Locate platelets.
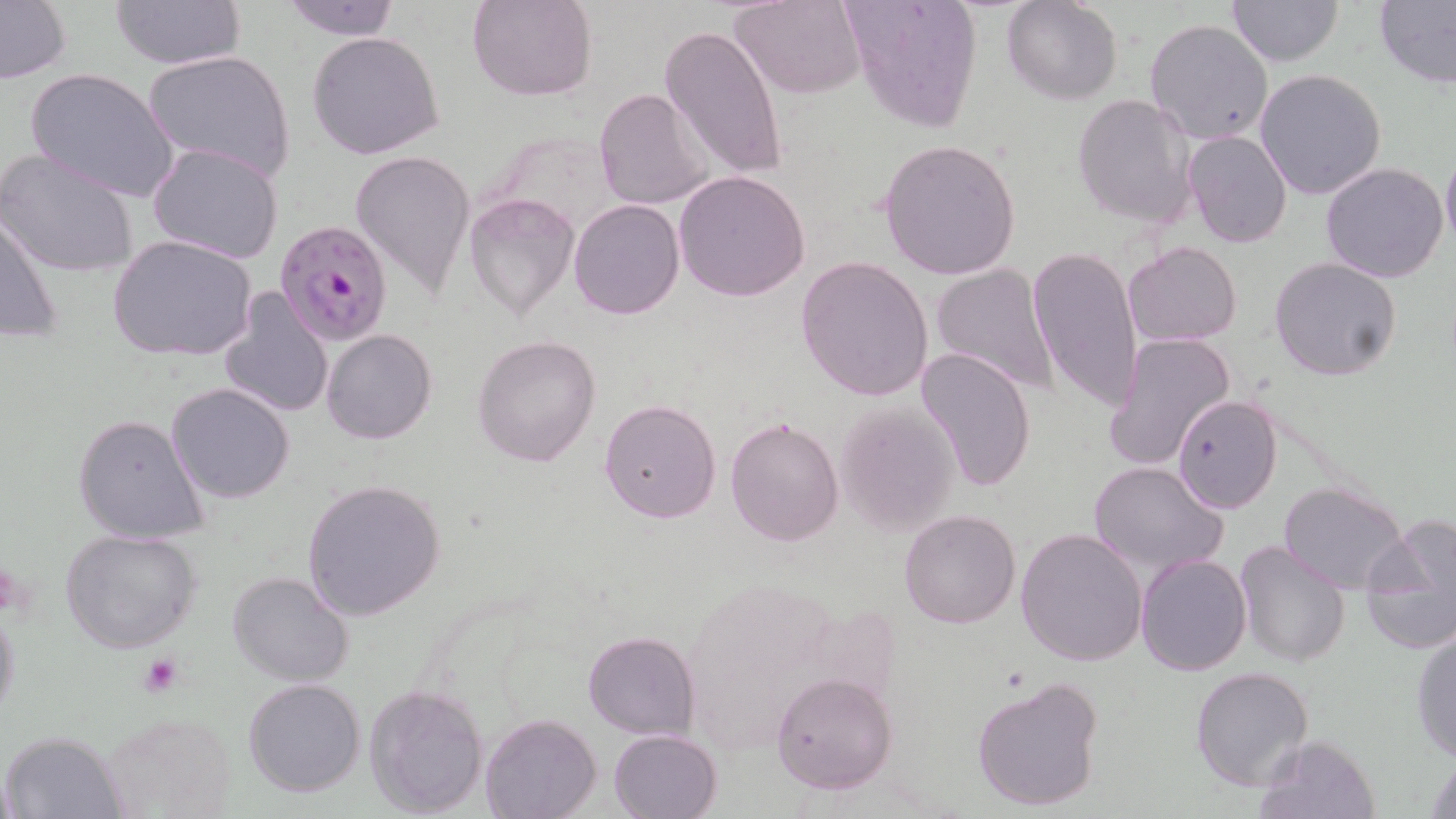

Approximate bounding boxes as (x1, y1, x2, y2) in pixels.
Platelets: (137, 653, 186, 698).

{
  "plasmodium_falciparum_infected_red_blood_cell_locations": "approximate bounding boxes as (x1, y1, x2, y2) in pixels: (275, 218, 396, 345)",
  "slide_level_diagnosis": "Plasmodium falciparum",
  "magnification": "1000x",
  "field_of_view": "single",
  "preparation": "thin blood smear",
  "uninfected_red_blood_cell_locations": "approximate bounding boxes as (x1, y1, x2, y2) in pixels: (108, 0, 246, 68), (279, 0, 401, 40), (468, 0, 598, 101), (731, 0, 867, 99), (841, 0, 984, 131), (1002, 0, 1123, 105), (1227, 0, 1344, 67), (1375, 0, 1456, 89), (0, 1, 71, 84), (1143, 18, 1274, 147), (660, 24, 789, 183), (306, 31, 445, 159), (142, 48, 296, 182), (26, 68, 180, 202), (1255, 68, 1387, 200), (592, 87, 714, 212), (1071, 94, 1197, 230), (1182, 128, 1293, 249), (877, 139, 1022, 280), (147, 143, 285, 265), (1, 147, 140, 279), (351, 148, 475, 296), (1440, 149, 1456, 251), (1320, 163, 1450, 283), (673, 169, 810, 302), (464, 192, 579, 320), (568, 199, 685, 320), (1, 206, 64, 347), (107, 235, 257, 362), (1124, 241, 1240, 347), (1027, 246, 1145, 413), (796, 255, 935, 402), (1269, 257, 1402, 382), (929, 263, 1061, 397), (218, 287, 334, 420), (321, 328, 436, 445), (1105, 332, 1237, 472), (471, 333, 603, 467), (915, 346, 1038, 491), (167, 382, 295, 503), (1172, 394, 1284, 514), (599, 398, 722, 523), (832, 401, 961, 535), (72, 414, 209, 544), (724, 417, 844, 545), (1087, 459, 1229, 576), (300, 478, 446, 620), (1278, 481, 1409, 593), (899, 508, 1020, 629), (1360, 517, 1456, 655), (59, 528, 201, 653), (1015, 528, 1148, 667), (1233, 540, 1354, 668), (1136, 554, 1253, 675), (226, 571, 354, 687), (0, 599, 20, 728), (1411, 628, 1456, 764), (583, 631, 698, 739), (1190, 667, 1313, 791), (771, 671, 897, 795), (972, 674, 1105, 814), (242, 678, 365, 798), (364, 684, 488, 816), (101, 710, 237, 816), (480, 714, 599, 819), (608, 729, 723, 819), (4, 731, 127, 818), (1255, 733, 1381, 819), (1425, 754, 1455, 818)",
  "image_size": "1456×819 pixels",
  "stain": "May-Grünwald-Giemsa",
  "modality": "light microscopy"
}